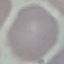

Malaria status: uninfected. Acquired by smartphone through the microscope eyepiece. Thin smear of blood. Automatically extracted cell patch, resized to 64 × 64 pixels. Giemsa-stained preparation.